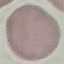
Summary:
  - Malaria status: uninfected
  - Stain: Giemsa
  - Capture: smartphone through the microscope eyepiece
  - Image type: automatically extracted cell patch, resized to 64 × 64 pixels
  - Preparation: thin blood film